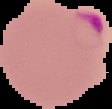 Image is 112×109 pixels. From a thin blood film. Cell region segmented out of the field of view; the surrounding area is masked to black. Malaria status: parasitized.